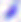

Summary:
  - Identification: Toxoplasma gondii
  - Modality: micrograph
  - Magnification: 400x